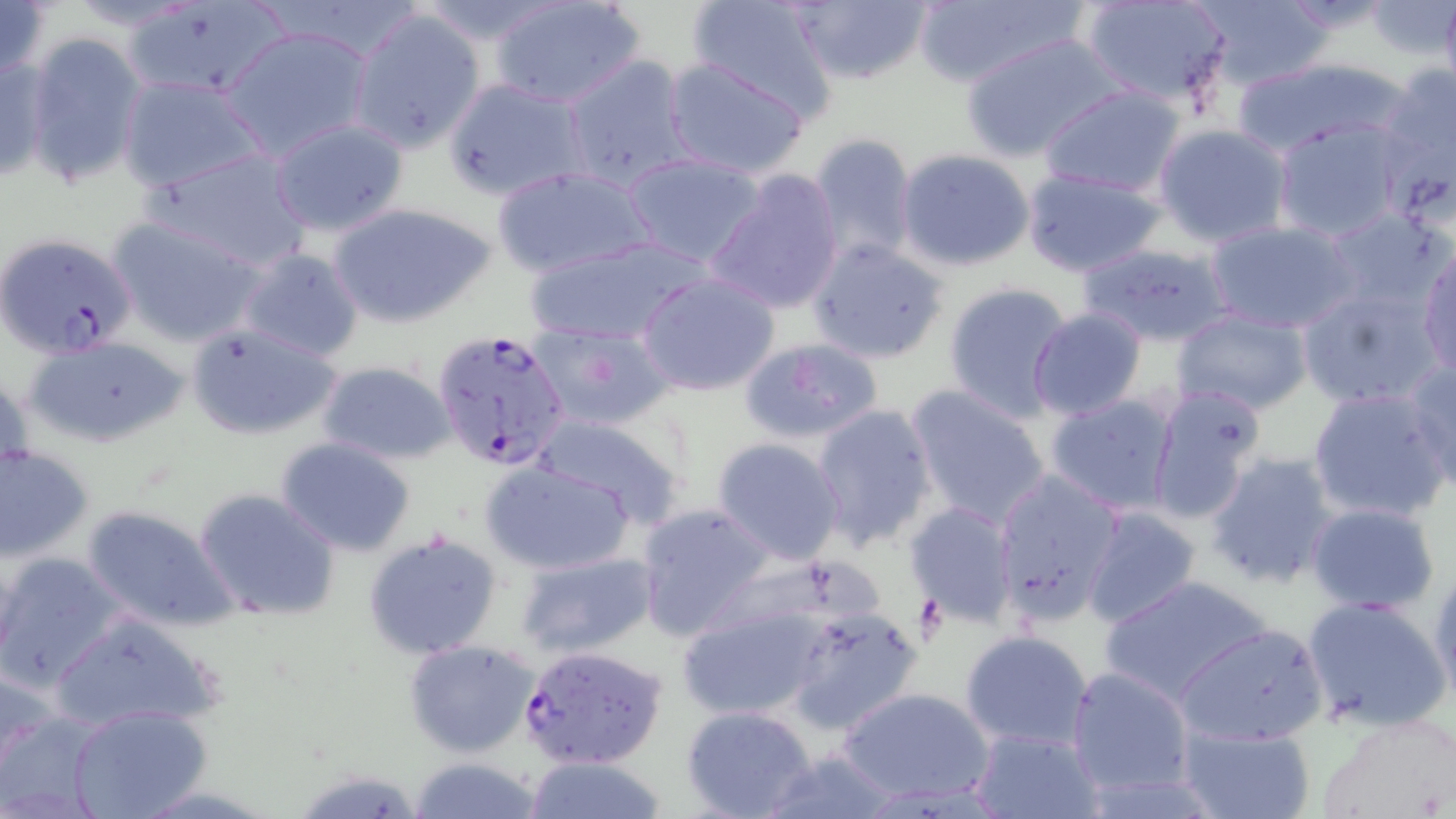
slide-level diagnosis = Plasmodium falciparum
uninfected red blood cell locations = approximate bounding boxes as [x1, y1, x2, y2] in pixels: [411, 0, 566, 44], [686, 0, 841, 121], [789, 0, 934, 86], [1081, 0, 1231, 108], [1192, 0, 1335, 91], [1, 1, 51, 81], [58, 1, 206, 33], [490, 1, 643, 108], [911, 1, 1088, 88], [122, 4, 290, 103], [346, 8, 487, 154], [219, 24, 375, 161], [23, 31, 147, 190], [960, 32, 1127, 161], [0, 52, 49, 185], [559, 54, 695, 192], [661, 55, 812, 178], [1230, 58, 1405, 156], [1373, 63, 1456, 200], [116, 75, 266, 195], [443, 78, 589, 201], [1039, 84, 1187, 197], [267, 118, 410, 237], [1271, 119, 1405, 243], [1153, 123, 1294, 249], [808, 133, 919, 266], [148, 147, 315, 272], [897, 148, 1035, 271], [623, 153, 766, 266], [491, 166, 655, 278], [1020, 166, 1168, 276], [704, 169, 845, 316], [327, 201, 498, 329], [1322, 208, 1450, 315], [108, 215, 265, 346], [1206, 220, 1359, 334], [804, 234, 950, 363], [523, 236, 708, 347], [1079, 241, 1234, 348], [236, 247, 365, 362], [1417, 247, 1456, 376], [636, 271, 782, 397], [941, 281, 1076, 422], [1296, 284, 1444, 411], [1026, 309, 1146, 422], [1171, 309, 1313, 416], [185, 321, 344, 442], [531, 322, 673, 430], [21, 335, 190, 449], [738, 337, 883, 447], [316, 359, 454, 464], [1404, 359, 1456, 488], [0, 369, 30, 496], [1145, 381, 1269, 526], [904, 383, 1054, 528], [1307, 387, 1452, 525], [1044, 393, 1181, 514], [809, 403, 938, 549], [529, 410, 686, 528], [275, 437, 416, 558], [712, 438, 846, 564], [0, 444, 94, 562], [1204, 451, 1339, 590], [479, 460, 635, 575], [992, 467, 1125, 625], [192, 486, 340, 623], [1305, 501, 1441, 614], [635, 502, 778, 641], [905, 502, 1018, 626], [79, 504, 236, 631], [1082, 507, 1203, 629], [363, 532, 505, 661], [513, 550, 659, 661], [0, 552, 128, 691], [1428, 561, 1456, 705], [1099, 574, 1278, 705], [1298, 595, 1452, 734], [673, 600, 839, 724], [780, 607, 924, 736], [47, 610, 224, 736], [1172, 622, 1328, 747], [958, 628, 1096, 751], [403, 638, 539, 758], [1065, 664, 1195, 798], [839, 685, 996, 805], [68, 704, 211, 819], [680, 706, 819, 818], [0, 709, 108, 818], [1322, 712, 1456, 819], [1173, 722, 1318, 819], [969, 726, 1104, 818], [756, 748, 902, 818], [406, 757, 547, 819], [518, 757, 672, 817]
modality = optical microscopy
magnification = 1000x
preparation = thin blood film
stain = May-Grünwald-Giemsa
image size = 1456×819 pixels
Plasmodium falciparum-infected red blood cell locations = approximate bounding boxes as [x1, y1, x2, y2] in pixels: [1, 230, 138, 357], [432, 328, 573, 474], [520, 643, 670, 771]
field of view = single